Describe the morphology of the erythrocytes.
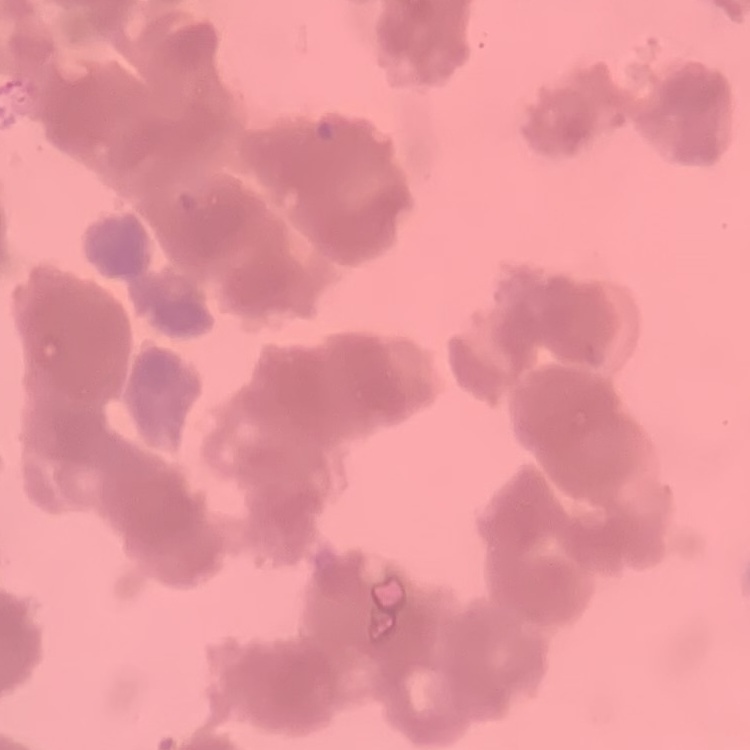

They show rouleaux formation.

preparation: thin blood film
stain: Field's or Giemsa
image_type: square crop of a larger photomicrograph